State the blood parasite species.
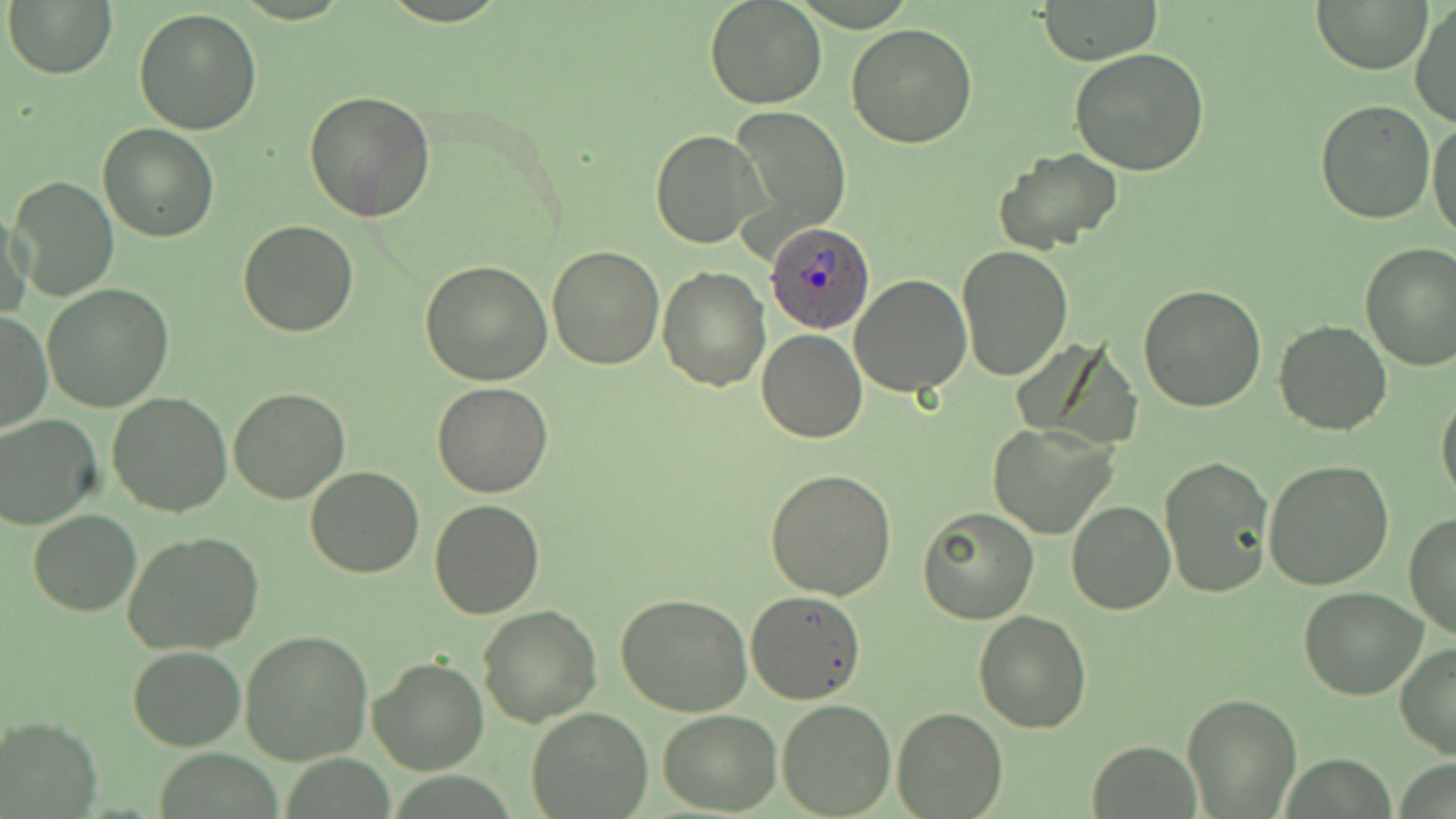
Plasmodium ovale.

Approximate bounding boxes as named x1/y1/x2/y2 corners in pixels. Plasmodium ovale-infected red blood cell locations: (x1=765, y1=224, x2=874, y2=337). Uninfected red blood cell locations: (x1=704, y1=0, x2=827, y2=109), (x1=1039, y1=0, x2=1163, y2=66), (x1=6, y1=1, x2=117, y2=79), (x1=1315, y1=1, x2=1430, y2=74), (x1=1410, y1=2, x2=1456, y2=128), (x1=134, y1=8, x2=262, y2=135), (x1=846, y1=22, x2=979, y2=149), (x1=1069, y1=48, x2=1209, y2=176), (x1=303, y1=90, x2=437, y2=225), (x1=1315, y1=99, x2=1435, y2=223), (x1=731, y1=106, x2=851, y2=237), (x1=1427, y1=119, x2=1456, y2=240), (x1=99, y1=123, x2=218, y2=242), (x1=650, y1=130, x2=765, y2=248), (x1=995, y1=146, x2=1124, y2=256), (x1=9, y1=176, x2=119, y2=301), (x1=1, y1=208, x2=32, y2=323), (x1=238, y1=219, x2=358, y2=336), (x1=1359, y1=243, x2=1456, y2=371), (x1=547, y1=245, x2=665, y2=369), (x1=956, y1=245, x2=1073, y2=379), (x1=421, y1=261, x2=553, y2=385), (x1=659, y1=266, x2=770, y2=389), (x1=848, y1=274, x2=970, y2=397), (x1=1137, y1=284, x2=1268, y2=412), (x1=41, y1=285, x2=174, y2=412), (x1=1, y1=308, x2=52, y2=434), (x1=1164, y1=309, x2=1393, y2=425), (x1=1273, y1=320, x2=1394, y2=435), (x1=757, y1=329, x2=867, y2=443), (x1=432, y1=382, x2=555, y2=498), (x1=228, y1=387, x2=351, y2=504), (x1=1436, y1=387, x2=1456, y2=507), (x1=106, y1=392, x2=234, y2=518), (x1=0, y1=414, x2=103, y2=530), (x1=988, y1=422, x2=1117, y2=539), (x1=1160, y1=453, x2=1273, y2=598), (x1=1263, y1=459, x2=1395, y2=591), (x1=766, y1=466, x2=898, y2=599), (x1=304, y1=467, x2=425, y2=578), (x1=429, y1=500, x2=546, y2=620), (x1=1067, y1=502, x2=1175, y2=616), (x1=917, y1=506, x2=1038, y2=623), (x1=29, y1=510, x2=140, y2=615), (x1=1404, y1=512, x2=1456, y2=641), (x1=122, y1=530, x2=267, y2=657), (x1=1299, y1=586, x2=1426, y2=699), (x1=745, y1=591, x2=866, y2=705), (x1=616, y1=596, x2=753, y2=716), (x1=477, y1=605, x2=602, y2=728), (x1=974, y1=609, x2=1091, y2=732), (x1=240, y1=631, x2=373, y2=765), (x1=1394, y1=641, x2=1456, y2=760), (x1=128, y1=645, x2=245, y2=751), (x1=368, y1=654, x2=490, y2=774), (x1=1184, y1=693, x2=1300, y2=816), (x1=777, y1=699, x2=896, y2=817), (x1=526, y1=706, x2=653, y2=819), (x1=894, y1=707, x2=1006, y2=817), (x1=658, y1=710, x2=783, y2=815), (x1=1, y1=715, x2=101, y2=817), (x1=1089, y1=741, x2=1200, y2=816). Optical microscopy. Thin blood film. May-Grünwald-Giemsa stain. Image is 1456×819 pixels. One field of a larger specimen. Captured at 1000x magnification.